Classify this cell by malaria status.
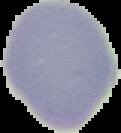

It is uninfected.

Summary:
  - Image size: 121×133 pixels
  - Preparation: thin blood smear
  - Image type: cell region segmented out of the field of view; surrounding area masked to black